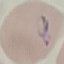
result = malaria parasites identified
preparation = thin blood smear
capture = smartphone camera at the microscope eyepiece
stain = Giemsa
image type = automatically extracted cell patch, resized to 64 × 64 pixels